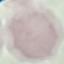
result: negative for malaria parasites
capture: smartphone camera at the microscope eyepiece
stain: Giemsa
image_type: automatically extracted cell patch, resized to 64 × 64 pixels
preparation: thin blood smear